Classify this cell by malaria status.
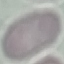

It is uninfected.

Summary:
  - Capture: smartphone camera at the microscope eyepiece
  - Image type: cell patch, automatically extracted from a larger field of view and resized to 64 × 64 pixels
  - Stain: Giemsa
  - Preparation: thin smear